Comment on the background quality.
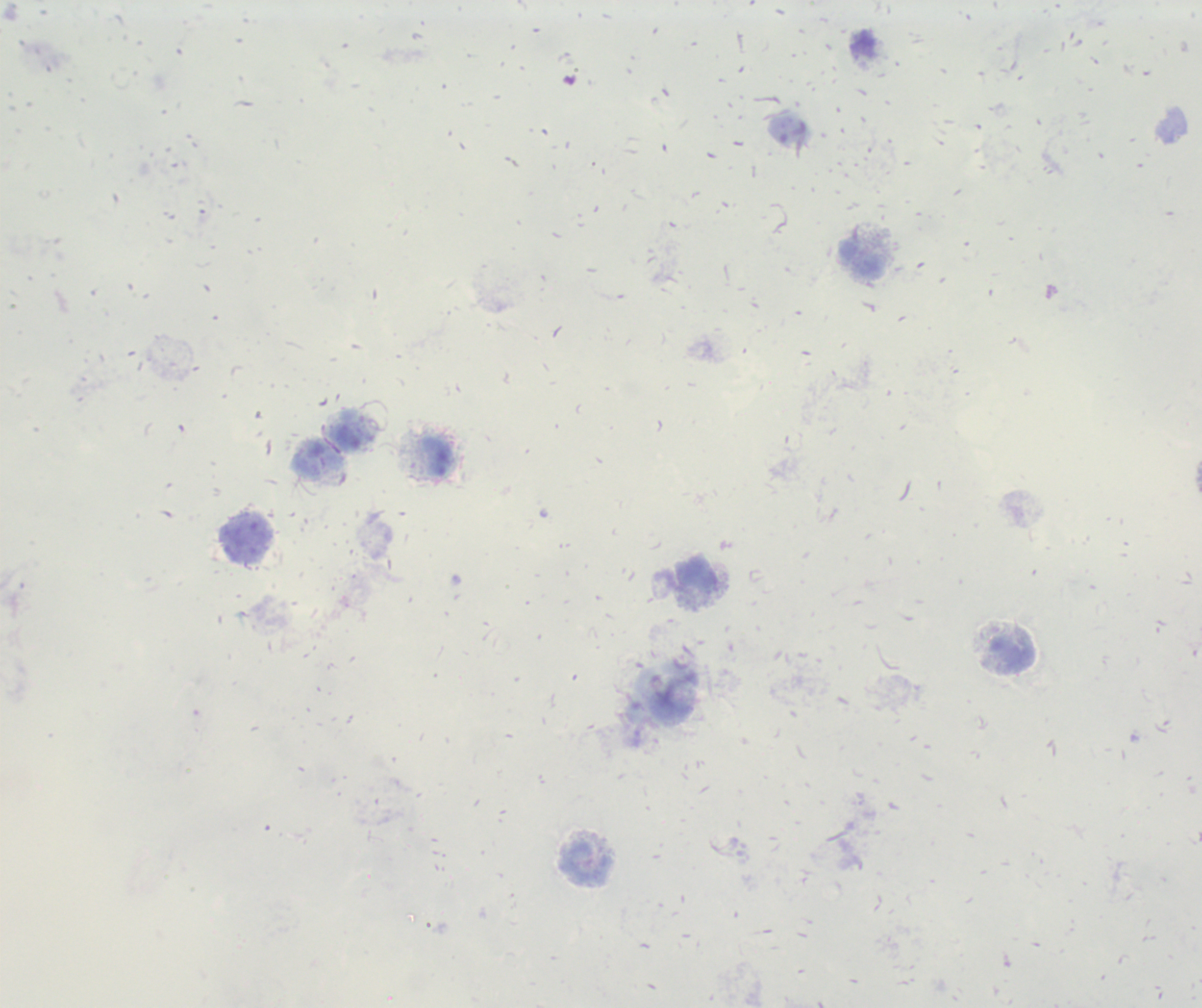

It is poor.

Approximate object centers, in pixels from the top-left corner. Leukocyte locations: (x=862, y=44), (x=437, y=456), (x=308, y=459), (x=1013, y=651), (x=587, y=863). Romanowsky stain. Result: negative for Plasmodium parasites. Thick blood smear. Previously used in a real diagnosis. Image is 1202×1008 pixels. Captured at 100x magnification. One field from this slide.